Outline each uninfected red blood cell.
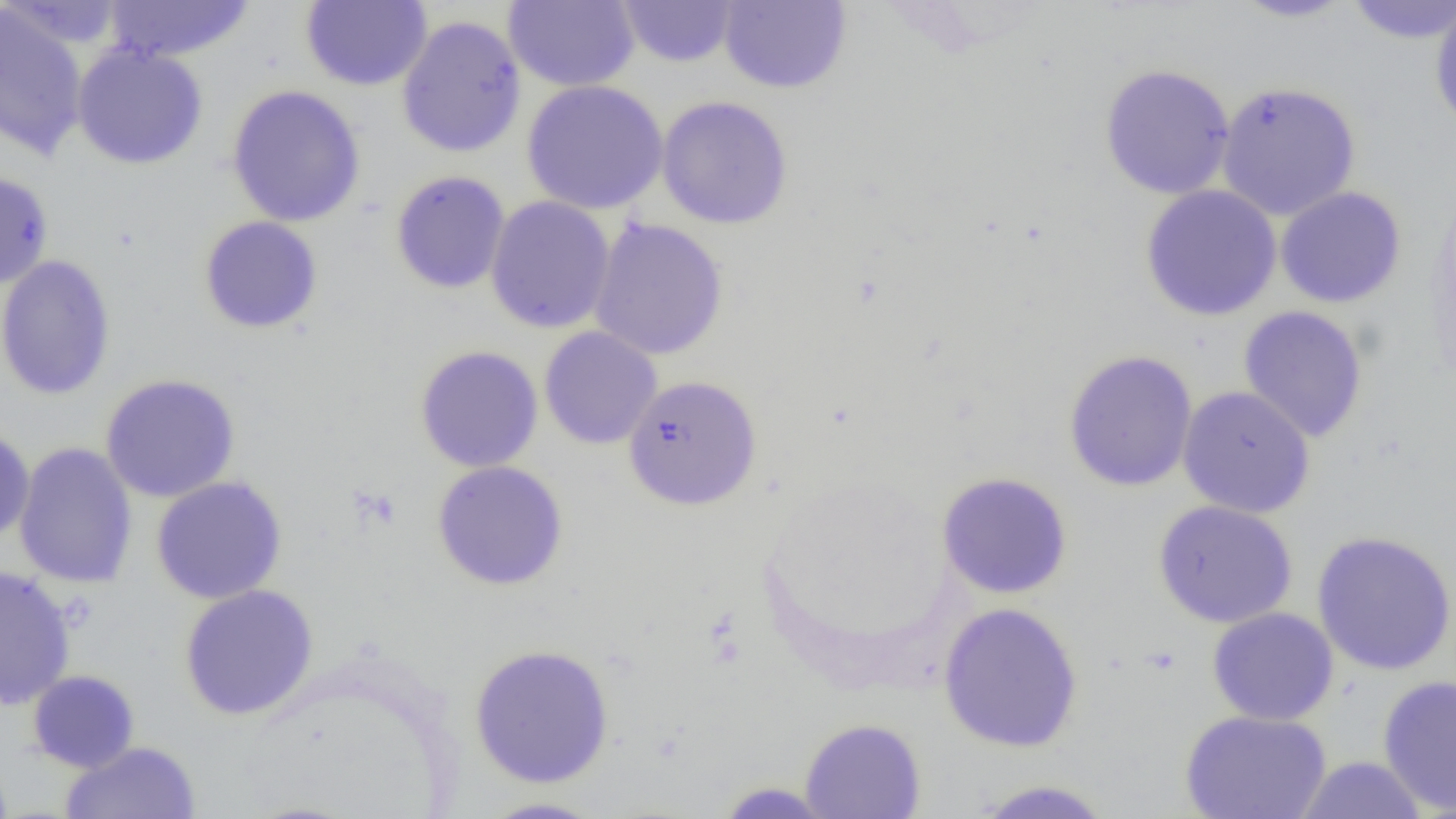

Approximate bounding boxes as (x1, y1, x2, y2) in pixels.
Uninfected red blood cells: (101, 0, 257, 64), (616, 0, 741, 67), (1230, 0, 1357, 23), (1343, 0, 1456, 44), (1429, 0, 1456, 133), (1, 1, 130, 50), (300, 1, 432, 91), (504, 1, 640, 91), (717, 1, 852, 94), (0, 4, 89, 161), (396, 14, 527, 158), (71, 43, 209, 170), (1098, 63, 1236, 200), (521, 79, 668, 215), (1216, 80, 1361, 220), (226, 84, 366, 228), (656, 95, 794, 230), (390, 169, 511, 294), (0, 170, 54, 289), (1140, 185, 1282, 321), (1275, 186, 1406, 308), (484, 196, 615, 334), (198, 216, 324, 334), (588, 217, 729, 361), (0, 254, 117, 401), (1238, 305, 1369, 443), (540, 329, 663, 452), (414, 345, 544, 473), (1063, 349, 1198, 492), (99, 373, 240, 502), (622, 374, 762, 510), (1177, 385, 1315, 518), (0, 425, 35, 544), (13, 441, 138, 589), (431, 460, 569, 591), (937, 471, 1073, 599), (151, 476, 287, 604), (1152, 500, 1298, 628), (1311, 530, 1456, 676), (0, 564, 76, 711), (178, 584, 319, 720), (938, 602, 1084, 753), (1207, 607, 1339, 725), (469, 643, 615, 788), (27, 669, 140, 773), (1377, 674, 1456, 816), (1179, 709, 1332, 819), (799, 717, 926, 818), (61, 740, 201, 819), (1293, 756, 1430, 818), (968, 778, 1117, 819), (713, 781, 838, 818), (474, 796, 612, 818).

Slide-level diagnosis: negative for blood parasites. Light microscopy. One field of a larger specimen. 1000x magnification. Image is 1456×819 pixels. Thin blood film.